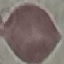

Summary:
  - Malaria status: uninfected
  - Image type: cell patch, automatically extracted from a larger field of view and resized to 64 × 64 pixels
  - Stain: Giemsa
  - Capture: smartphone camera at the microscope eyepiece
  - Preparation: thin blood film